Report the malaria status of this cell.
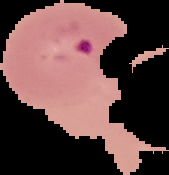
Parasitized.

Image is 169×175 pixels. From a thin blood film. Cell region segmented out of the field of view; the surrounding area is masked to black.